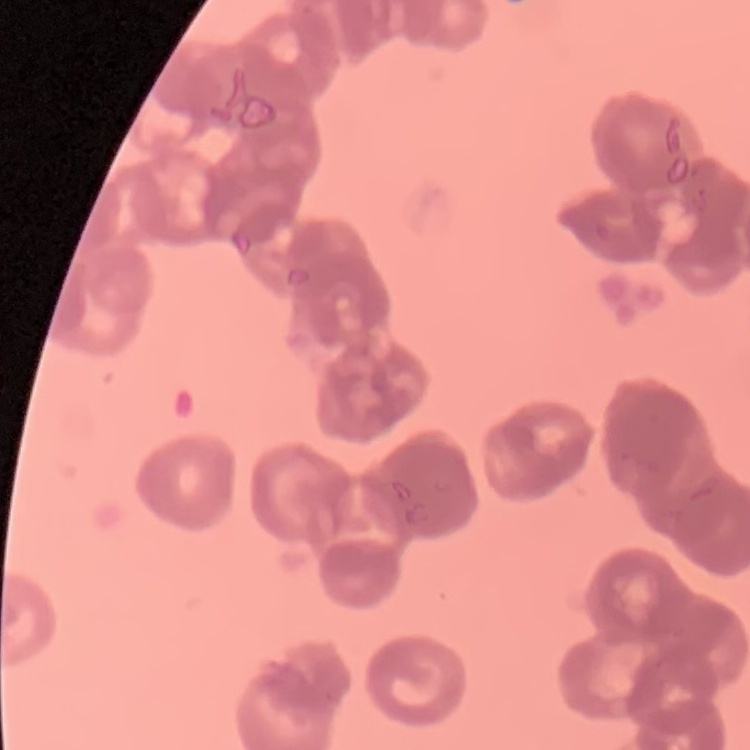

Summary:
  - Erythrocyte morphology: rouleaux formation
  - Stain: Field's or Giemsa
  - Preparation: thin blood film
  - Image type: one tile cut from a larger photomicrograph